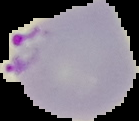
From a thin blood smear. Image is 139×121 pixels. The area outside the segmented cell region is set to black. Result: Plasmodium parasites identified.